Name the parasite shown.
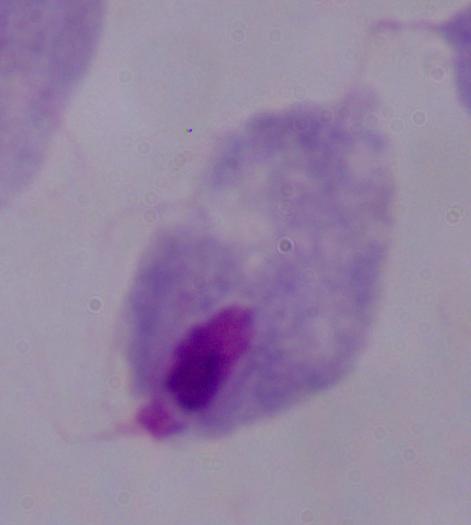

This is a trichomonad.

modality = photomicrograph
magnification = 1000x